Assess this cell for malaria.
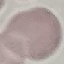
It is uninfected.

Summary:
  - Stain: Giemsa
  - Image type: cell patch, automatically extracted from a larger field of view and resized to 64 × 64 pixels
  - Preparation: thin blood film
  - Capture: smartphone camera at the microscope eyepiece